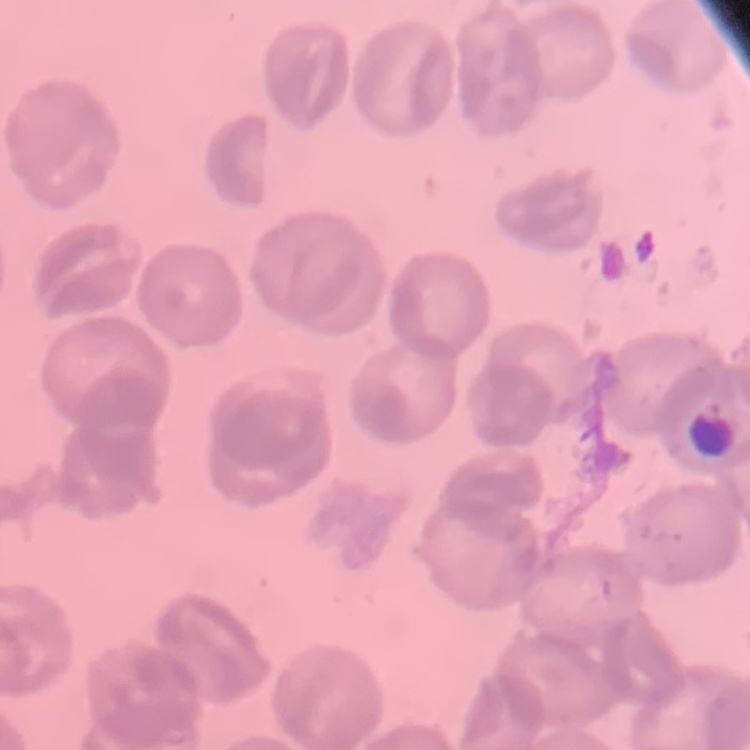

red_blood_cell_morphology: no rouleaux formation
image_type: square crop of a larger photomicrograph
preparation: thin peripheral smear
stain: Field's or Giemsa